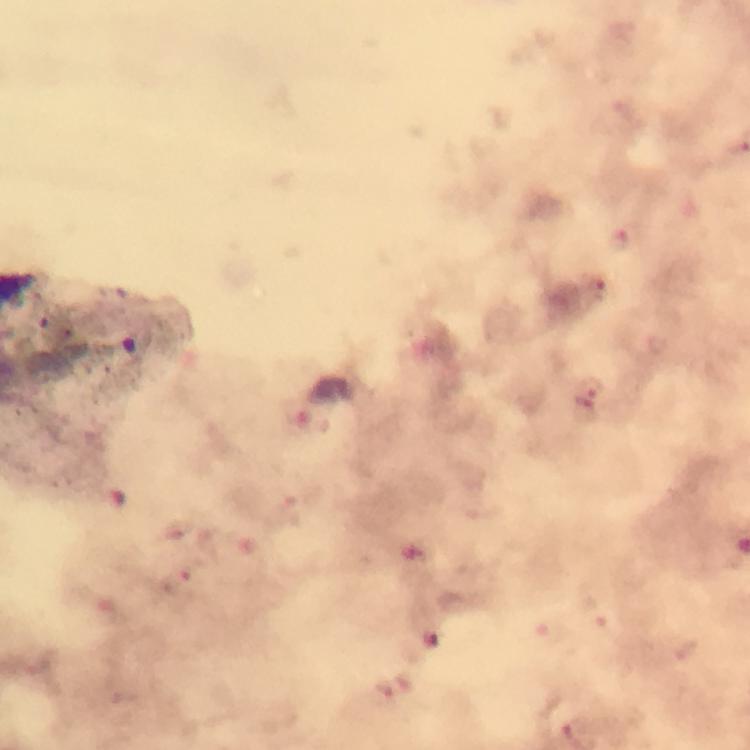
Approximate centers as (x, y) in pixels.
Summary:
  - Malaria parasite locations: (622, 239), (601, 287), (590, 395), (181, 587), (432, 639), (395, 687)
  - Magnification: 100x
  - Context: from a diagnostic examination for malaria
  - Stain: Giemsa
  - Capture: smartphone mounted on the microscope
  - Cropped from: a single field of view
  - Image size: 750×750 pixels
  - Preparation: thick blood film
  - Immersion oil: used